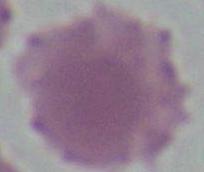
magnification = 1000x
identification = erythrocyte
modality = photomicrograph